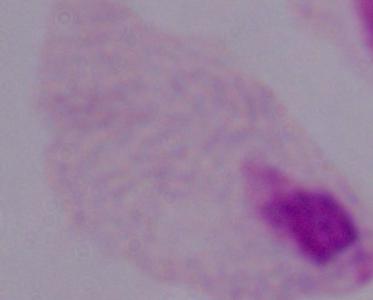

modality: micrograph
identification: trichomonad
magnification: 1000x